Give the extent of all Plasmodium vivax-infected red blood cells.
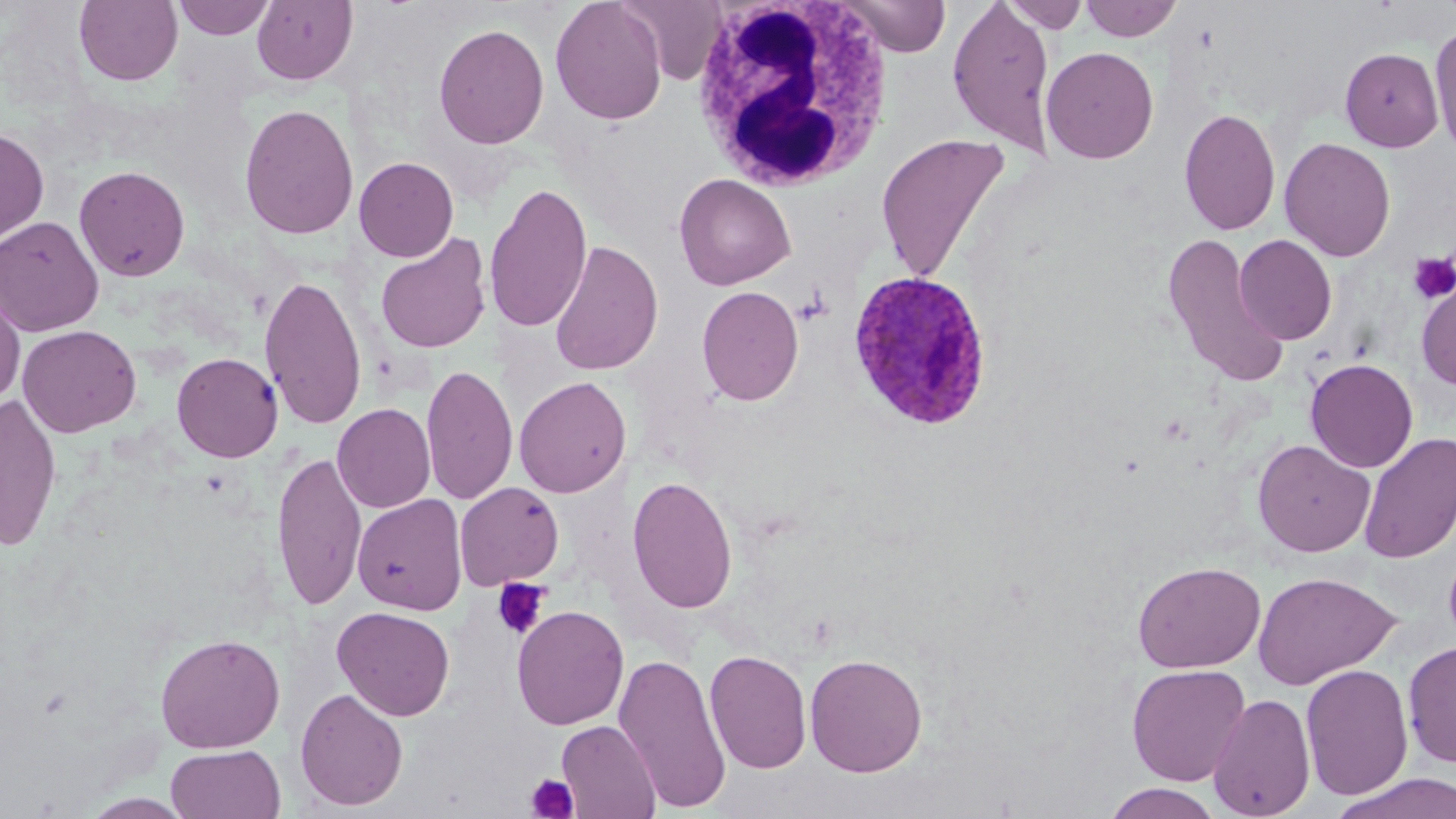

Approximate bounding boxes as [x1, y1, x2, y2] in pixels.
Plasmodium vivax-infected red blood cells: [847, 270, 994, 432].

Uninfected red blood cell locations: [173, 0, 275, 40], [251, 0, 358, 86], [550, 0, 667, 125], [620, 0, 725, 85], [837, 0, 953, 57], [947, 0, 1056, 156], [1079, 0, 1184, 42], [74, 1, 183, 87], [1001, 1, 1089, 33], [1430, 22, 1456, 160], [433, 23, 549, 149], [1041, 46, 1159, 164], [1340, 47, 1444, 152], [239, 103, 359, 240], [1178, 107, 1280, 236], [0, 126, 50, 245], [875, 132, 1011, 282], [1279, 137, 1396, 262], [353, 156, 458, 262], [74, 164, 191, 282], [674, 173, 796, 290], [484, 181, 593, 333], [0, 216, 104, 336], [1161, 231, 1290, 389], [375, 233, 492, 354], [1234, 235, 1337, 345], [549, 240, 664, 376], [260, 274, 367, 430], [1416, 278, 1456, 392], [0, 284, 26, 407], [697, 285, 804, 405], [17, 324, 142, 437], [172, 352, 283, 462], [1305, 358, 1418, 473], [421, 363, 518, 505], [514, 376, 631, 498], [0, 393, 62, 552], [332, 403, 436, 513], [1358, 432, 1456, 565], [1252, 439, 1375, 557], [271, 451, 367, 610], [627, 475, 738, 613], [454, 482, 564, 590], [352, 494, 467, 615], [1132, 560, 1267, 673], [1252, 571, 1401, 689], [511, 605, 629, 730], [332, 606, 455, 721], [155, 631, 286, 753], [1402, 641, 1456, 768], [704, 649, 813, 774], [613, 652, 731, 812], [805, 653, 928, 777], [1126, 663, 1251, 786], [1300, 663, 1414, 801], [294, 687, 408, 812], [1208, 693, 1316, 817], [556, 719, 661, 818], [165, 745, 285, 819], [1330, 772, 1456, 819], [1101, 783, 1226, 818], [81, 793, 193, 818]. White blood cell locations: [688, 0, 895, 190]. Platelet locations: [1408, 253, 1456, 305], [492, 578, 550, 639], [526, 772, 578, 817]. Slide-level diagnosis: Plasmodium vivax. Image is 1456×819 pixels. One field of a larger specimen. May-Grünwald-Giemsa-stained preparation. Captured at 1000x magnification. Light microscopy. Thin blood smear.